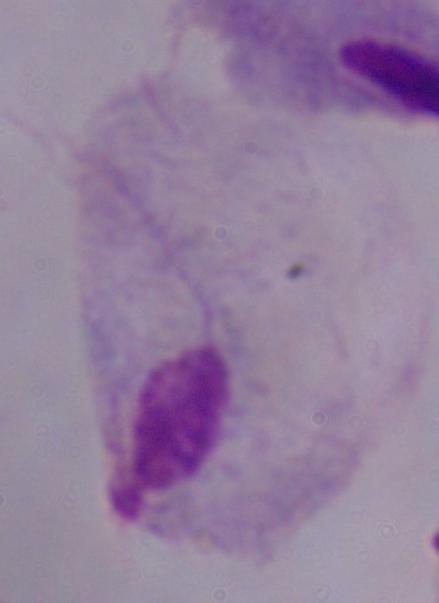

modality = photomicrograph
magnification = 1000x
identification = trichomonad